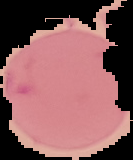
Summary:
  - Malaria status: uninfected
  - Preparation: thin blood smear
  - Image size: 133×160 pixels
  - Image type: segmented cell region with the area outside set to black